Comment on the morphology of the red blood cells.
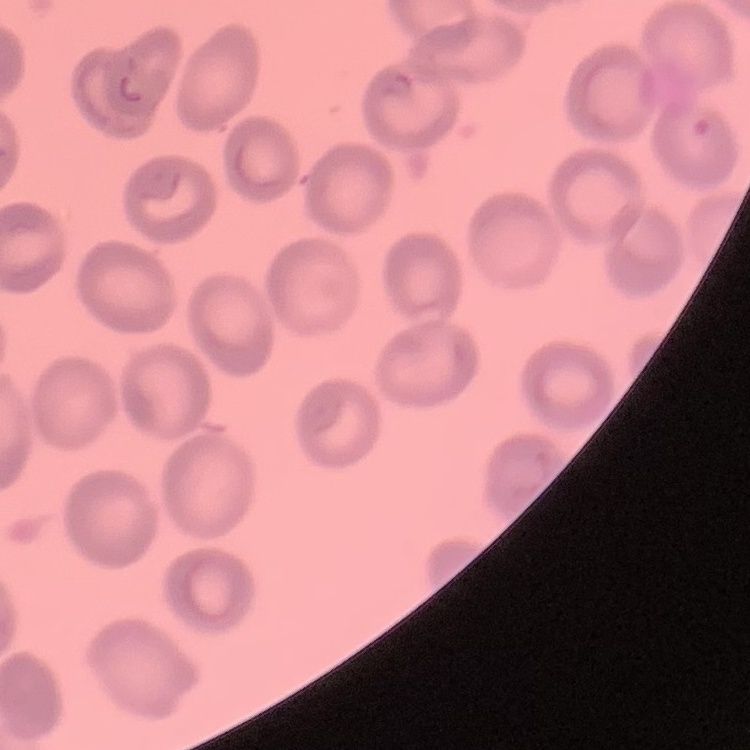
No rouleaux formation.

Summary:
  - Image type: one tile cut from a larger photomicrograph
  - Stain: Field's or Giemsa
  - Preparation: thin peripheral smear